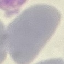

Summary:
  - Malaria status: uninfected
  - Image type: automatically extracted cell patch, resized to 64 × 64 pixels
  - Preparation: thin blood smear
  - Stain: Giemsa
  - Capture: smartphone camera at the microscope eyepiece